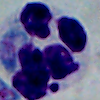

Summary:
  - Identification: white blood cell
  - Magnification: 1000x
  - Modality: photomicrograph